Point out each Plasmodium parasite.
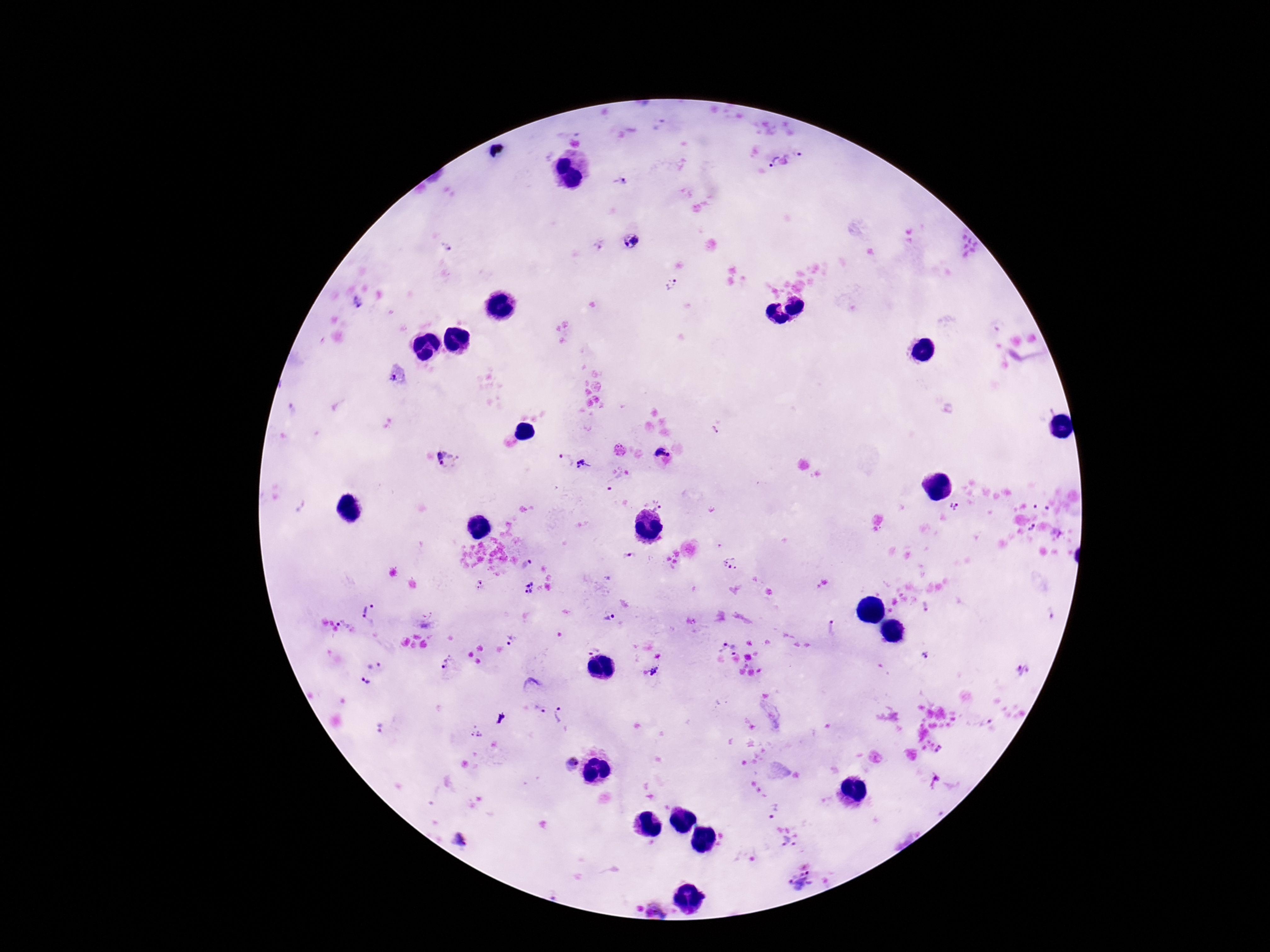
Approximate centers as (x, y) in pixels.
Plasmodium parasites: (794, 156), (771, 161), (620, 182), (631, 240), (601, 245), (671, 283), (358, 303), (397, 378), (715, 430), (620, 450), (661, 455), (565, 459), (449, 463), (582, 464), (657, 506), (956, 507), (1034, 528), (627, 556), (529, 562), (731, 563), (480, 582), (479, 588), (529, 588), (924, 606), (373, 607), (365, 611), (1052, 612), (428, 615), (610, 618), (339, 623), (831, 627), (511, 640), (722, 644), (592, 648), (736, 649), (926, 656), (448, 661), (375, 666), (655, 671), (1024, 671), (365, 681), (540, 710), (561, 714), (981, 724), (381, 730), (475, 732), (941, 750), (572, 763), (773, 810), (785, 841), (458, 842), (800, 881), (658, 909).

100x magnification. Image is 1270×952 pixels. Patient malaria status: infected. One field from this slide. Giemsa-stained preparation. Thick blood smear. Smartphone photograph taken through the microscope eyepiece.